Mark where platelets are.
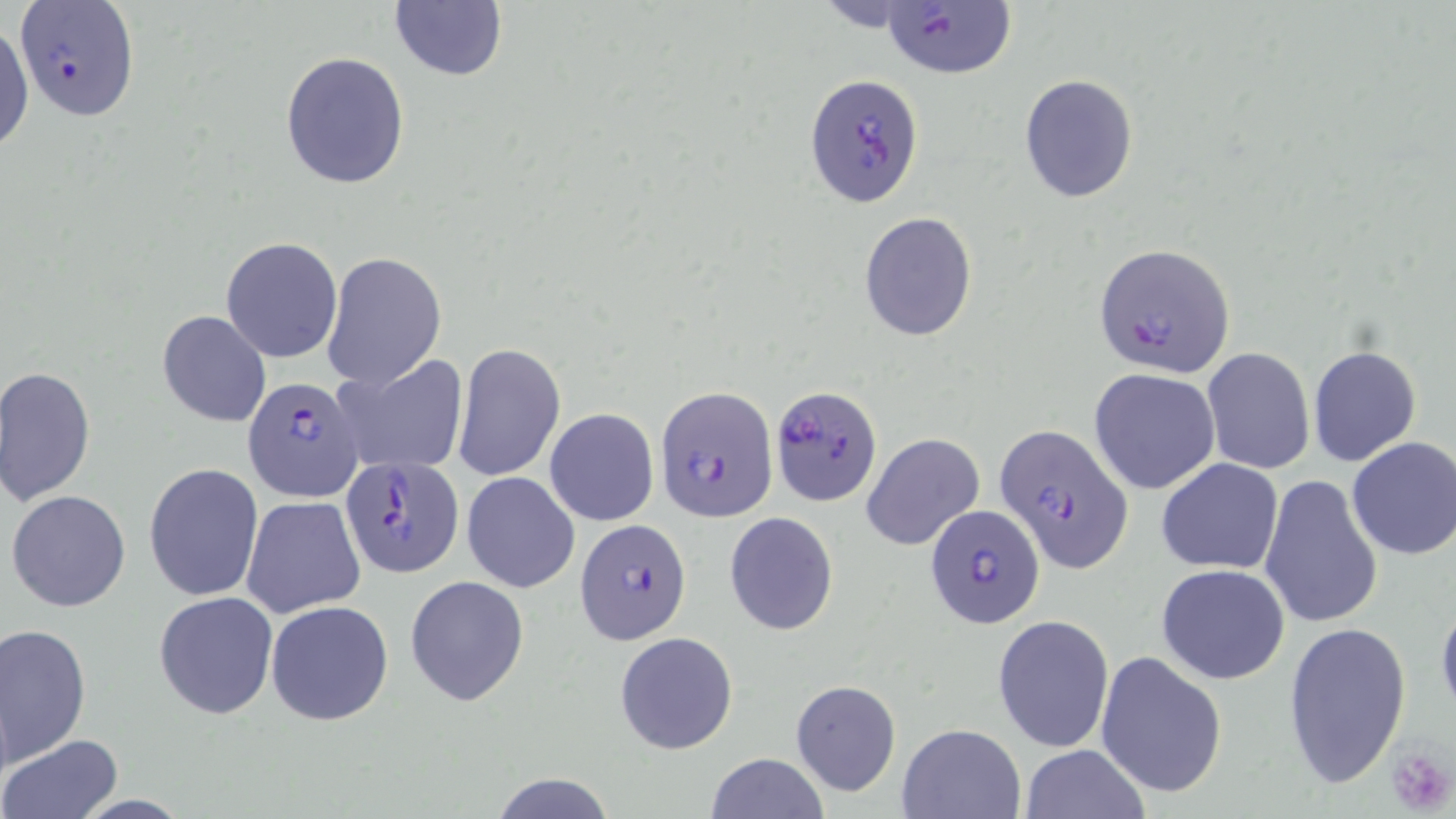
Approximate bounding boxes as named x1/y1/x2/y2 corners in pixels.
Platelets: (x1=1386, y1=745, x2=1455, y2=817).

slide-level diagnosis = Plasmodium falciparum
image size = 1456×819 pixels
field of view = one of a larger specimen
modality = optical microscopy
magnification = 1000x
stain = May-Grünwald-Giemsa
Plasmodium falciparum-infected red blood cell locations (subset) = approximate bounding boxes as named x1/y1/x2/y2 corners in pixels: (x1=879, y1=1, x2=1016, y2=80), (x1=805, y1=71, x2=924, y2=207), (x1=1092, y1=242, x2=1235, y2=379), (x1=243, y1=378, x2=365, y2=503), (x1=770, y1=383, x2=883, y2=505), (x1=656, y1=387, x2=778, y2=521), (x1=996, y1=423, x2=1134, y2=574), (x1=340, y1=454, x2=465, y2=579), (x1=923, y1=502, x2=1046, y2=629), (x1=576, y1=518, x2=692, y2=644)
uninfected red blood cell locations (subset) = approximate bounding boxes as named x1/y1/x2/y2 corners in pixels: (x1=388, y1=2, x2=507, y2=83), (x1=0, y1=22, x2=33, y2=158), (x1=280, y1=51, x2=410, y2=189), (x1=1018, y1=73, x2=1139, y2=204), (x1=858, y1=211, x2=978, y2=342), (x1=220, y1=236, x2=342, y2=363), (x1=322, y1=252, x2=447, y2=391), (x1=157, y1=309, x2=272, y2=427), (x1=450, y1=343, x2=565, y2=482), (x1=1307, y1=345, x2=1421, y2=466), (x1=1202, y1=347, x2=1315, y2=474), (x1=334, y1=356, x2=467, y2=475), (x1=2, y1=366, x2=97, y2=504), (x1=1089, y1=369, x2=1220, y2=493), (x1=544, y1=408, x2=659, y2=527), (x1=861, y1=431, x2=984, y2=552), (x1=1346, y1=436, x2=1456, y2=561), (x1=1156, y1=459, x2=1284, y2=574), (x1=144, y1=462, x2=265, y2=601), (x1=461, y1=473, x2=579, y2=592), (x1=1259, y1=474, x2=1383, y2=630), (x1=6, y1=490, x2=131, y2=612), (x1=240, y1=495, x2=366, y2=618), (x1=725, y1=512, x2=838, y2=635), (x1=1156, y1=563, x2=1291, y2=684), (x1=405, y1=576, x2=530, y2=706), (x1=154, y1=590, x2=278, y2=721), (x1=1436, y1=598, x2=1456, y2=723), (x1=265, y1=599, x2=393, y2=726), (x1=993, y1=614, x2=1114, y2=753), (x1=1281, y1=619, x2=1412, y2=794), (x1=0, y1=622, x2=91, y2=770), (x1=614, y1=631, x2=739, y2=756), (x1=1096, y1=651, x2=1227, y2=800), (x1=791, y1=679, x2=902, y2=798), (x1=898, y1=724, x2=1024, y2=818), (x1=2, y1=735, x2=122, y2=817), (x1=1020, y1=744, x2=1149, y2=819), (x1=705, y1=752, x2=830, y2=818), (x1=491, y1=773, x2=617, y2=818)
preparation = thin blood film